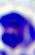
magnification = 400x
modality = micrograph
identification = white blood cell